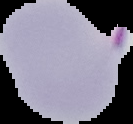 Segmented cell region on a black background. Malaria status: parasitized. Image is 133×124 pixels. From a thin blood smear.